Identify the parasite.
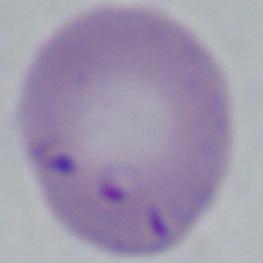

This is Babesia.

Captured at 1000x magnification. Photomicrograph.